Describe the morphology of the red blood cells.
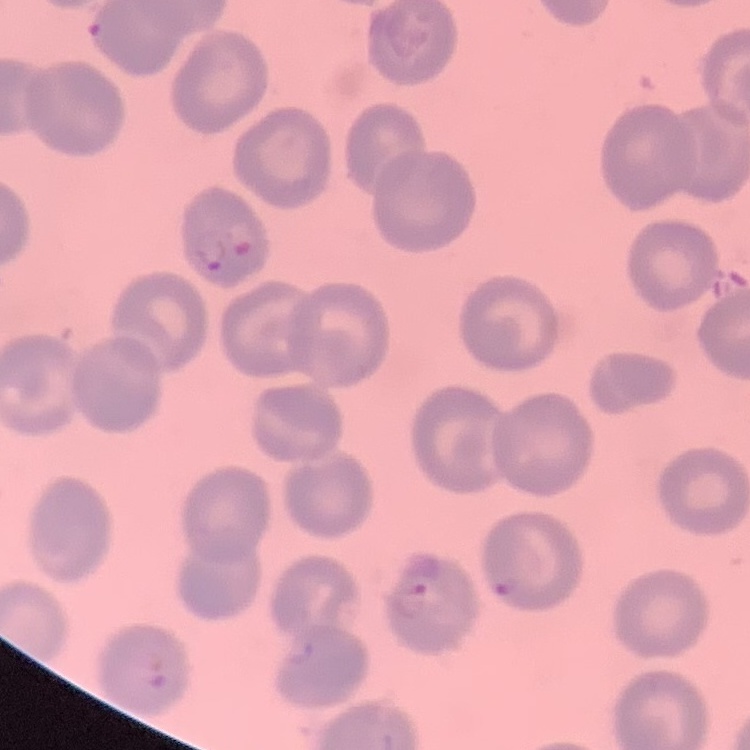
No rouleaux formation.

stain = Field's or Giemsa
image type = one tile cut from a larger photomicrograph
preparation = thin blood smear